Describe the morphology of the red blood cells.
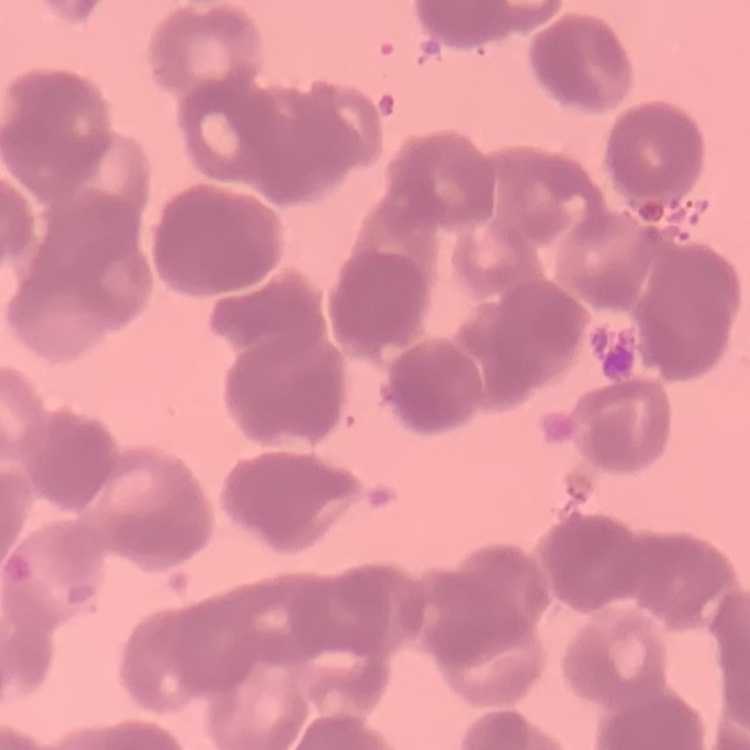
Rouleaux formation.

preparation = thin blood smear
image type = one tile cut from a larger photomicrograph
stain = Field's or Giemsa